Locate every blood parasite and identify its species.
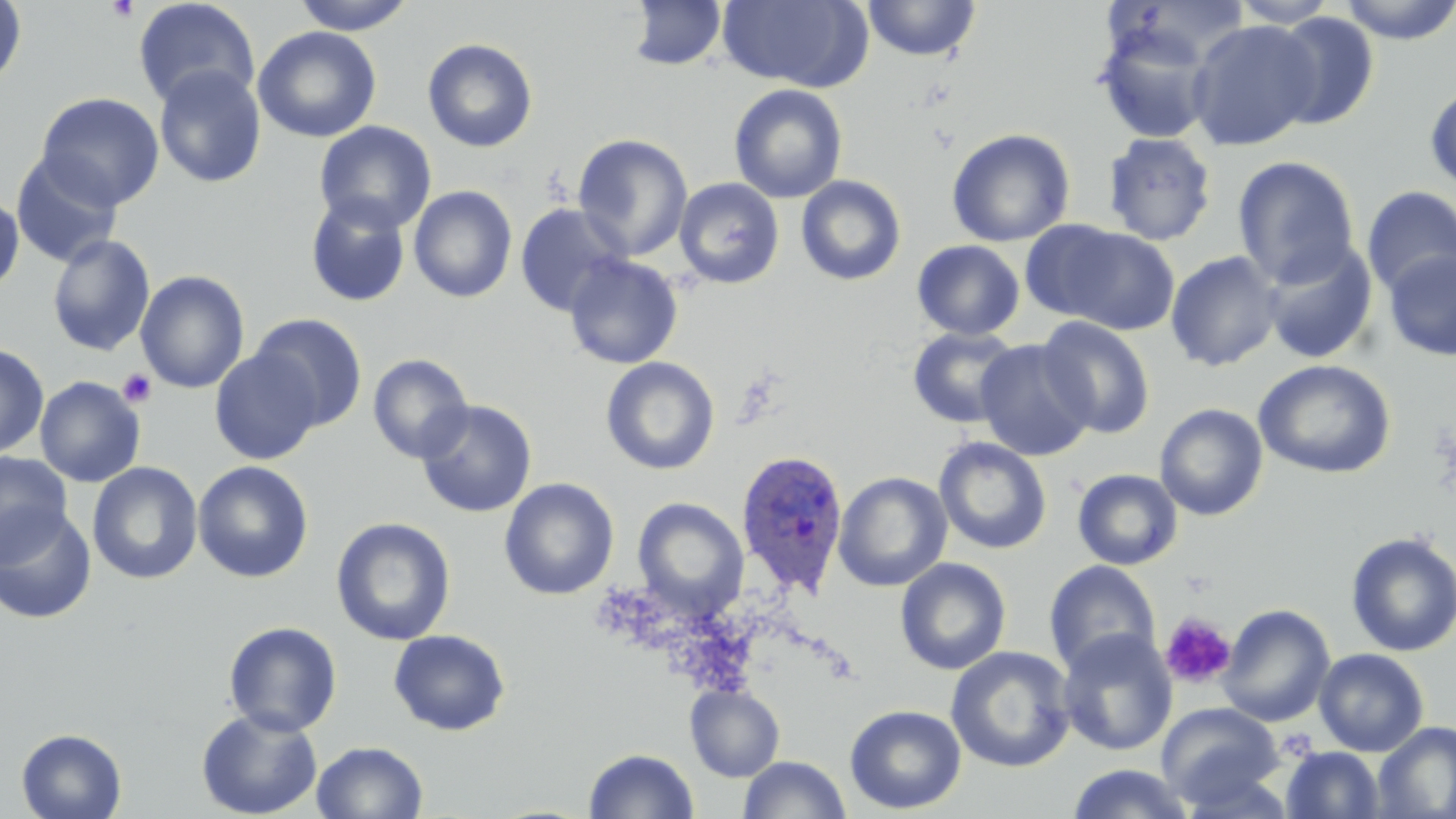
Approximate bounding boxes as [x1, y1, x2, y2] in pixels.
Plasmodium ovale-infected red blood cells: [735, 449, 850, 595].
No Plasmodium falciparum, Plasmodium malariae, Plasmodium vivax, Babesia divergens, or Trypanosoma brucei observed.

slide-level diagnosis = Plasmodium ovale
magnification = 1000x
uninfected red blood cell locations = approximate bounding boxes as [x1, y1, x2, y2] in pixels: [132, 0, 261, 111], [291, 0, 418, 34], [627, 0, 727, 71], [717, 0, 872, 91], [862, 0, 981, 61], [1229, 0, 1339, 27], [1337, 0, 1456, 45], [0, 1, 27, 90], [1268, 11, 1380, 130], [1187, 19, 1321, 150], [1093, 22, 1217, 144], [253, 26, 381, 143], [422, 38, 538, 153], [153, 66, 267, 188], [729, 83, 848, 204], [1425, 84, 1456, 195], [35, 92, 165, 211], [314, 121, 437, 234], [947, 128, 1075, 247], [1102, 132, 1218, 246], [573, 134, 693, 260], [11, 153, 124, 269], [1232, 155, 1360, 288], [795, 175, 907, 286], [674, 177, 785, 289], [409, 186, 517, 303], [1360, 186, 1456, 298], [0, 191, 24, 294], [305, 194, 411, 307], [515, 203, 632, 316], [1018, 220, 1133, 323], [1051, 225, 1181, 335], [46, 234, 155, 356], [912, 239, 1025, 341], [1260, 241, 1378, 364], [1165, 250, 1284, 372], [1381, 250, 1456, 361], [564, 254, 684, 369], [135, 270, 250, 393], [248, 313, 368, 433], [1036, 316, 1156, 438], [907, 326, 1024, 429], [975, 340, 1096, 461], [0, 342, 49, 460], [209, 348, 323, 465], [367, 353, 474, 464], [600, 356, 720, 475], [1253, 359, 1397, 479], [34, 376, 145, 487], [415, 399, 537, 518], [1154, 403, 1268, 521], [934, 436, 1052, 555], [0, 451, 73, 564], [192, 460, 314, 583], [87, 461, 203, 584], [1071, 468, 1182, 570], [833, 471, 953, 591], [499, 478, 619, 600], [632, 497, 749, 620], [0, 508, 97, 624], [331, 517, 456, 646], [1345, 531, 1456, 657], [895, 557, 1011, 675], [1044, 561, 1162, 676], [1217, 604, 1336, 727], [224, 621, 343, 736], [388, 629, 511, 735], [1057, 629, 1177, 756], [945, 645, 1076, 773], [1314, 648, 1429, 756], [685, 684, 785, 782], [1157, 702, 1284, 809], [845, 704, 967, 814], [196, 707, 322, 819], [1373, 721, 1456, 818], [16, 728, 127, 819], [311, 740, 428, 819], [1282, 746, 1385, 818], [584, 748, 698, 819], [740, 755, 850, 818], [1066, 764, 1197, 819]
field of view = single
platelet locations = approximate bounding boxes as [x1, y1, x2, y2] in pixels: [106, 0, 139, 23], [117, 368, 157, 408], [1160, 613, 1237, 689], [1275, 732, 1320, 764]
image size = 1456×819 pixels
preparation = thin blood smear
modality = light microscopy
stain = May-Grünwald-Giemsa